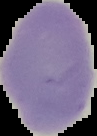
Summary:
  - Preparation: thin blood film
  - Malaria status: uninfected
  - Image size: 97×136 pixels
  - Image type: cell region segmented out of the field of view; surrounding area masked to black